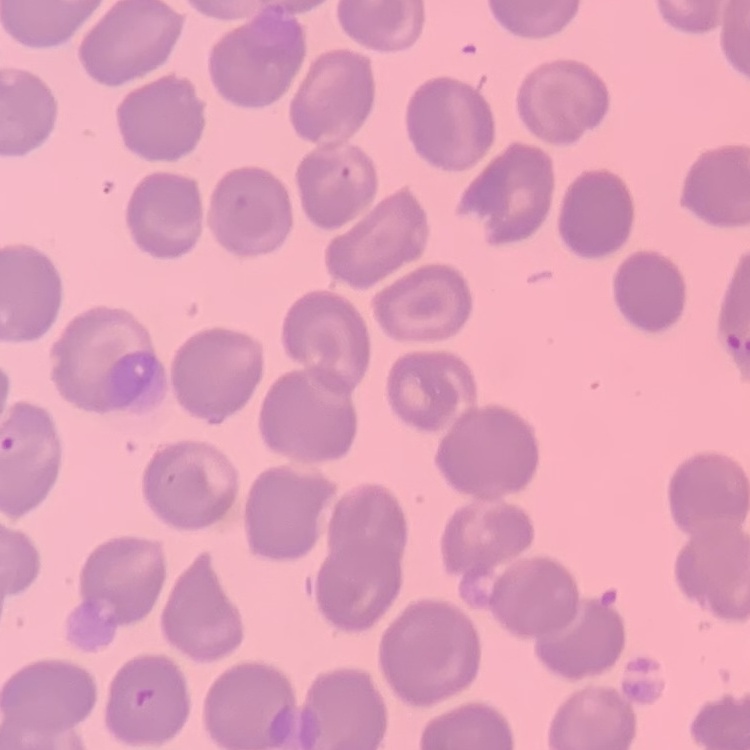
erythrocyte morphology = no rouleaux formation
preparation = thin peripheral smear
stain = Field's or Giemsa
image type = square crop of a larger photomicrograph